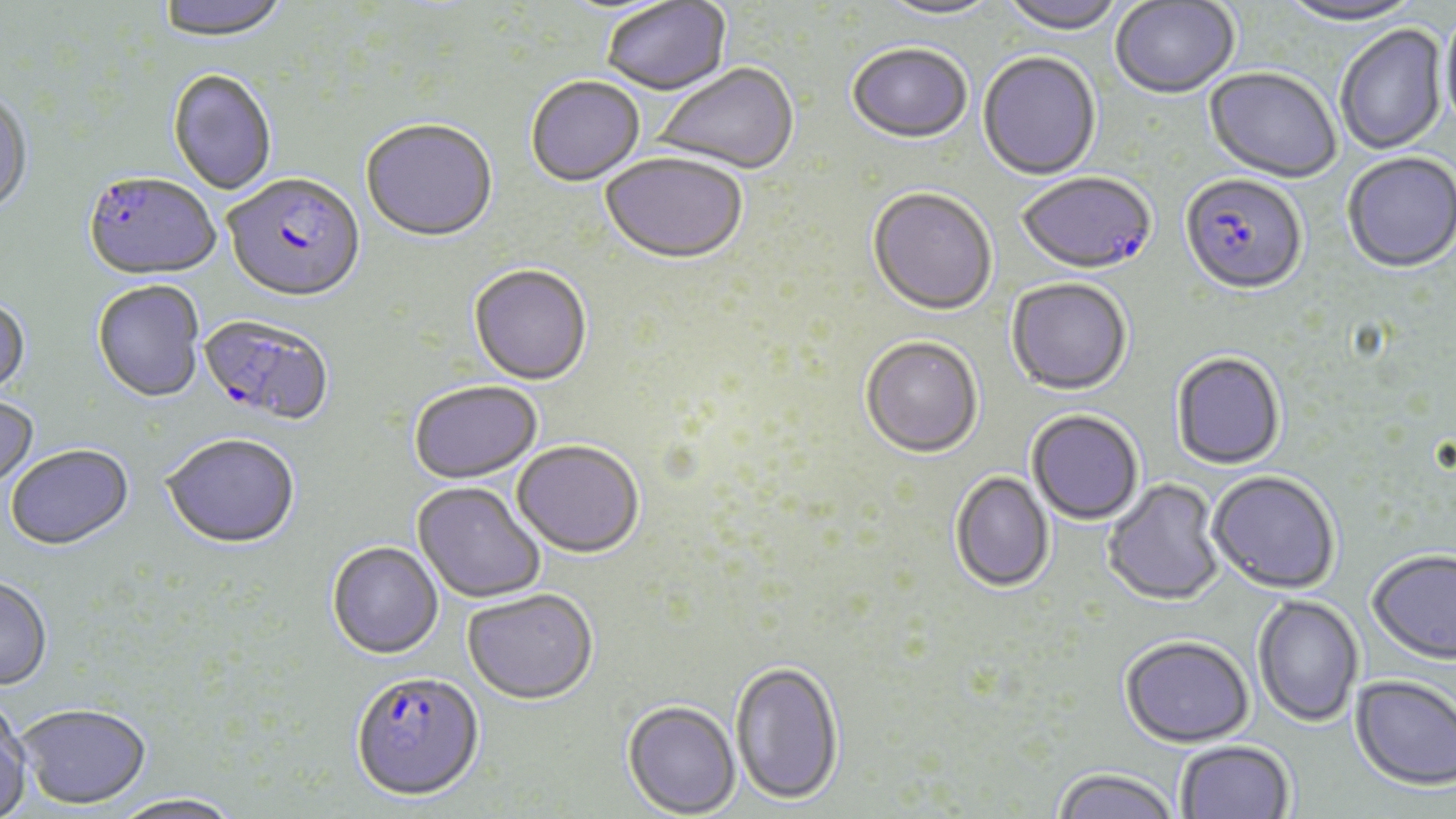 Approximate bounding boxes as (x1,y1)-(x2,y2) corner pairs in pixels. Uninfected red blood cell locations: (156,0)-(289,47), (999,0)-(1125,37), (875,1)-(1004,23), (1110,1)-(1239,100), (1277,1)-(1424,28), (602,2)-(732,98), (1439,11)-(1456,137), (1335,25)-(1448,156), (846,46)-(973,146), (978,54)-(1101,182), (652,65)-(799,177), (1203,69)-(1341,186), (167,70)-(277,196), (525,78)-(645,188), (0,91)-(33,220), (360,122)-(499,246), (1342,154)-(1456,275), (600,155)-(748,267), (867,190)-(997,318), (468,266)-(592,387), (1006,279)-(1132,397), (92,281)-(204,405), (0,298)-(30,400), (860,339)-(983,460), (1171,353)-(1285,471), (408,383)-(544,486), (0,395)-(39,495), (1027,411)-(1144,526), (162,436)-(301,551), (511,443)-(645,560), (5,447)-(135,552), (950,471)-(1055,593), (1207,471)-(1340,595), (1102,479)-(1226,607), (412,483)-(546,605), (327,543)-(444,661), (1367,551)-(1456,666), (0,578)-(53,692), (463,590)-(599,706), (1252,594)-(1364,728), (1120,636)-(1254,747), (730,661)-(844,806), (1350,675)-(1456,791), (623,700)-(740,817), (0,702)-(32,818), (17,706)-(152,810), (1175,740)-(1295,819), (1051,768)-(1179,819), (109,795)-(246,819). Plasmodium falciparum-infected red blood cell locations: (1018,173)-(1157,278), (82,174)-(220,283), (223,174)-(366,306), (1180,176)-(1308,298), (198,315)-(334,429), (350,672)-(484,803). Slide-level diagnosis: Plasmodium falciparum. Captured at 1000x magnification. One field of a larger specimen. Thin blood smear. Image is 1456×819 pixels. May-Grünwald-Giemsa stain. Optical microscopy.